Report the malaria status of this cell.
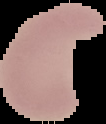

It is parasitized.

preparation = thin blood film
image size = 106×124 pixels
image type = cell region segmented out of the field of view; surrounding area masked to black